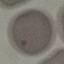

result = no malaria parasites detected
stain = Giemsa
preparation = thin blood smear
capture = smartphone through the microscope eyepiece
image type = cell patch, automatically extracted from a larger field of view and resized to 64 × 64 pixels